Describe the morphology of the red blood cells.
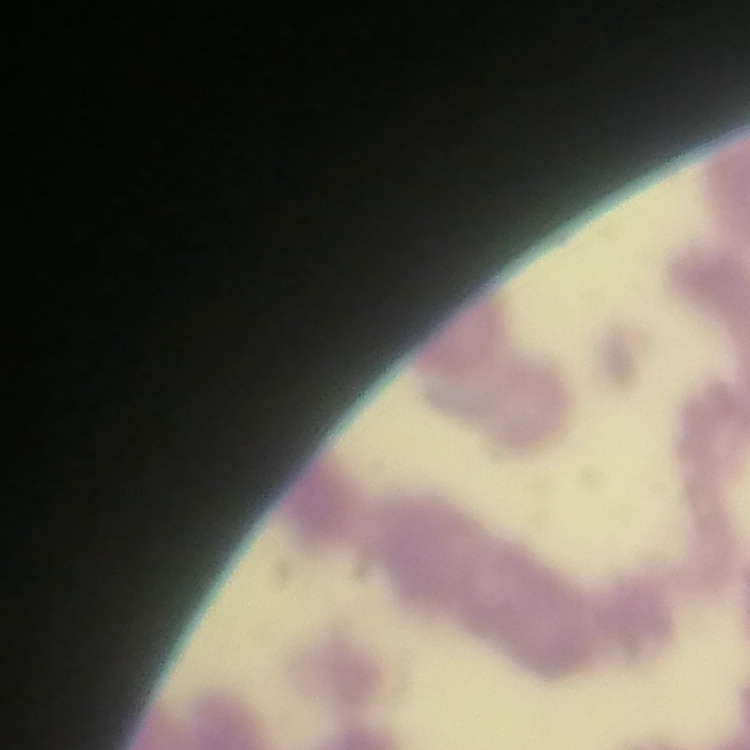
They show rouleaux formation.

stain = Field's or Giemsa
image type = one tile cut from a larger photomicrograph
preparation = thin blood smear